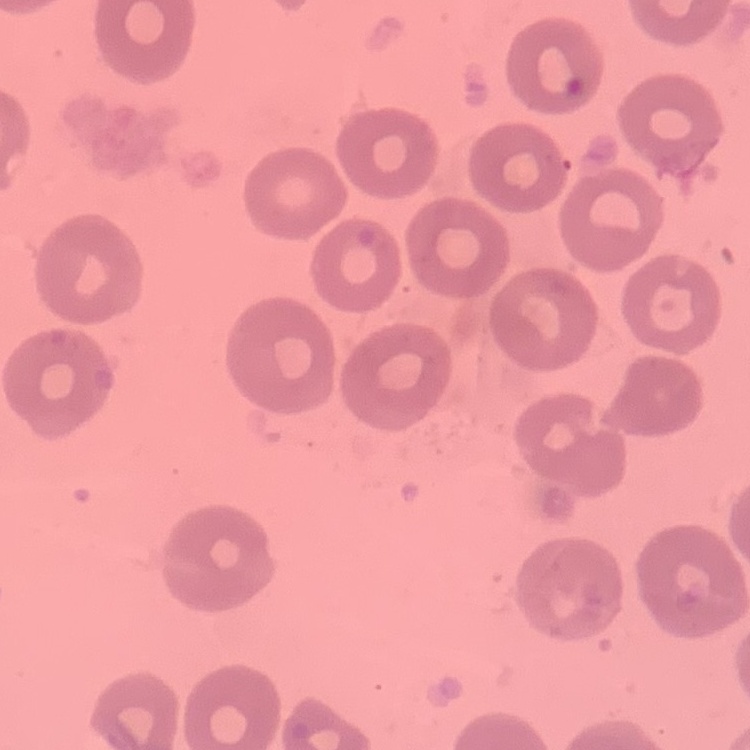 The red blood cells exhibit no rouleaux formation. Thin blood film. Square crop of a larger photomicrograph. Stained with either Field's or Giemsa.